Assess the morphology of the red blood cells.
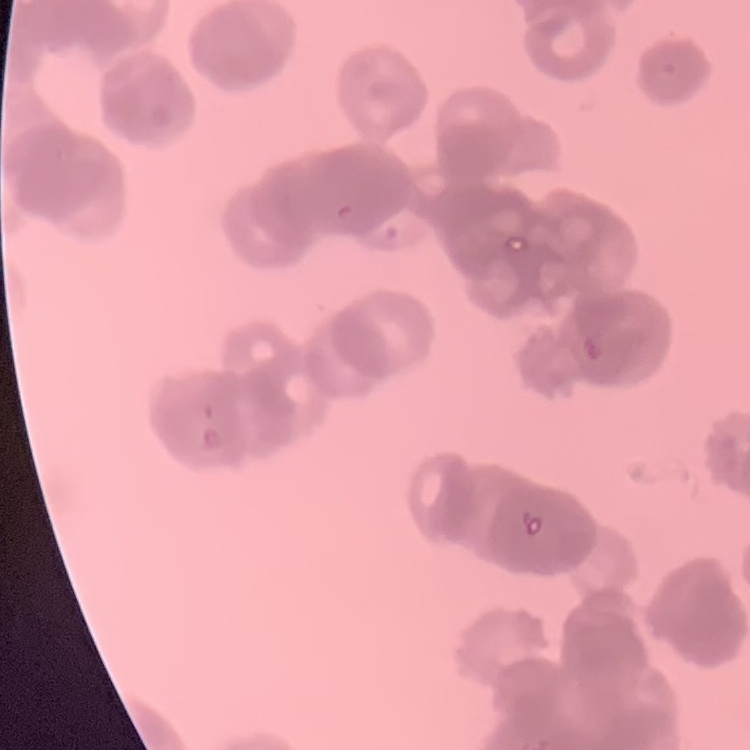

Rouleaux formation.

Summary:
  - Preparation: thin blood smear
  - Stain: Field's or Giemsa
  - Image type: square crop of a larger photomicrograph